Describe the morphology of the red blood cells.
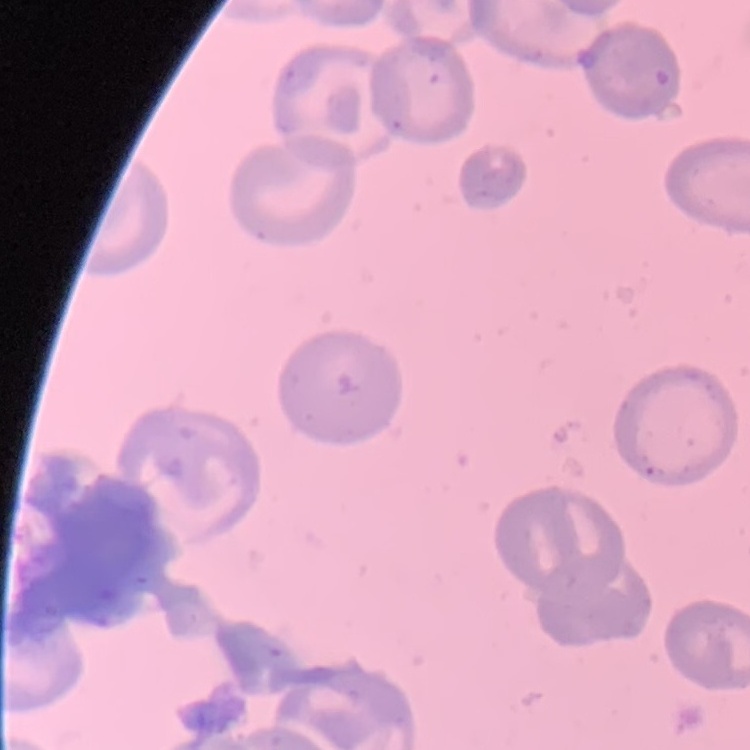
They show no rouleaux formation.

Summary:
  - Stain: Field's or Giemsa
  - Preparation: thin blood film
  - Image type: square crop of a larger photomicrograph